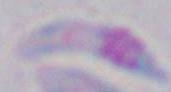

Toxoplasma gondii is seen. Captured at 1000x magnification. Photomicrograph.